Evaluate for parasitized red blood cells.
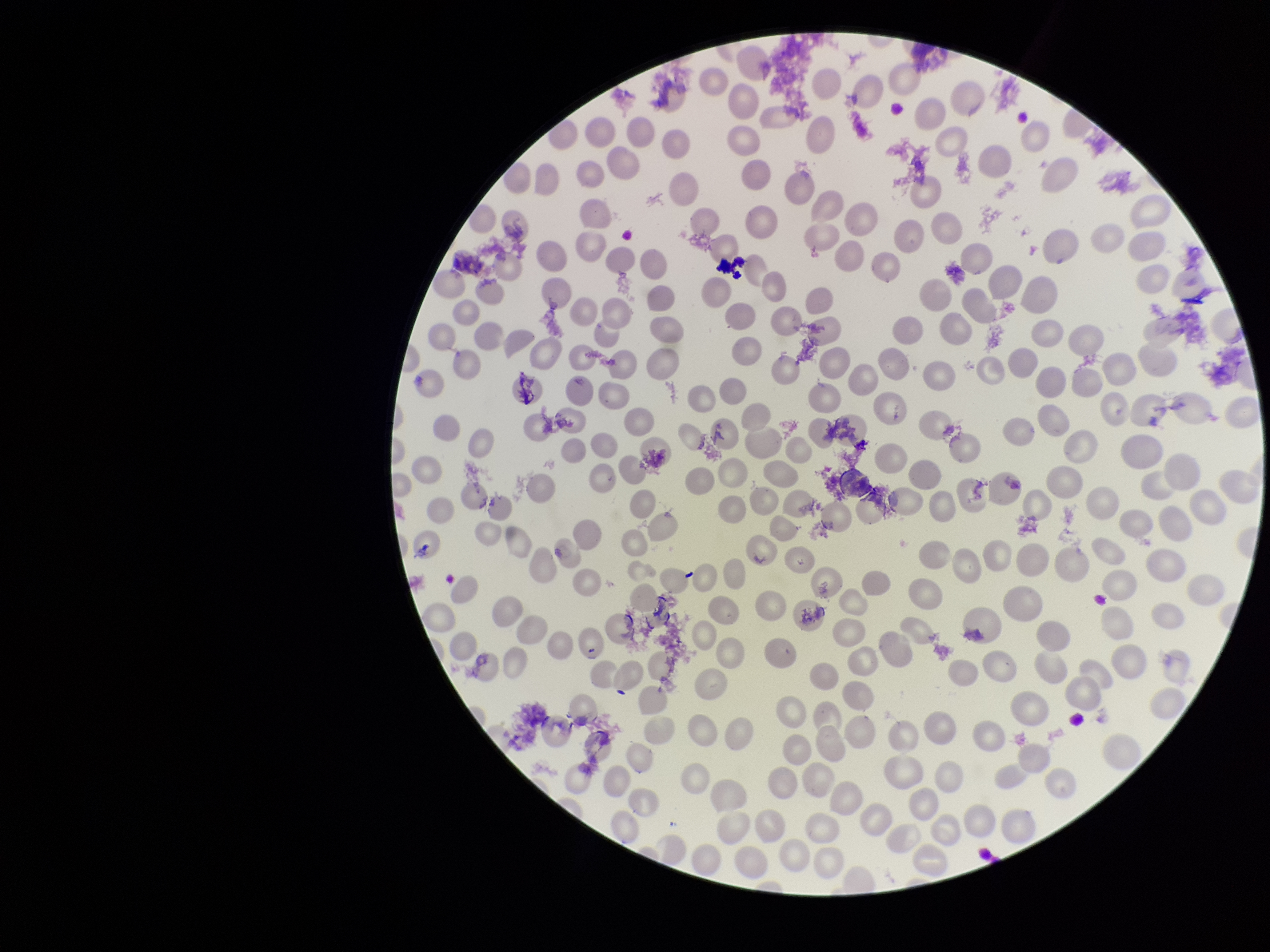

None detected.

Patient malaria status: negative. Preparation: thin. Red blood cell count: 237. Parasitized red blood cell count: 0. Image is 1270×952 pixels. Single field of view. Photographed through the microscope eyepiece with a smartphone camera. Stained with Giemsa.